Assess this cell for malaria.
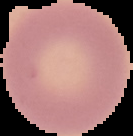
Uninfected.

Cell region segmented out of the field of view; the surrounding area is masked to black. From a thin blood film. Image is 133×136 pixels.